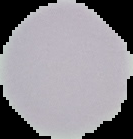
Summary:
  - Malaria status: uninfected
  - Image size: 133×139 pixels
  - Image type: segmented cell region on a black background
  - Preparation: thin blood film